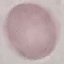 Malaria status: uninfected. Acquired by smartphone through the microscope eyepiece. Automatically extracted cell patch, resized to 64 × 64 pixels. Thin blood smear. Giemsa stain.